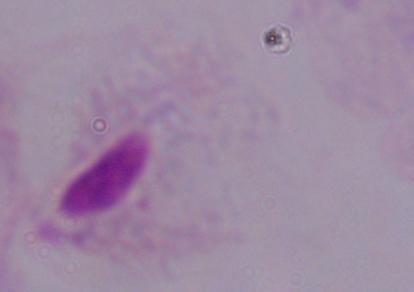
magnification: 1000x
identification: trichomonad
modality: micrograph